Identify the parasite.
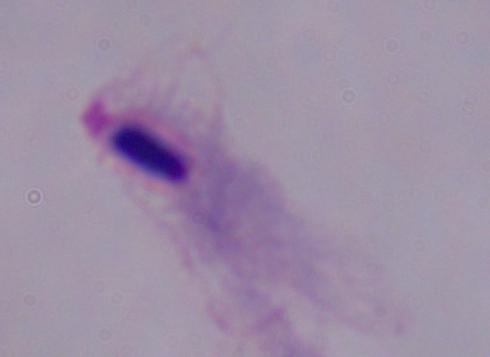
A trichomonad.

Captured at 1000x magnification. Photomicrograph.